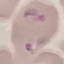

Result: malaria parasites detected. Acquired by smartphone through the microscope eyepiece. Cell patch, automatically extracted from a larger field of view and resized to 64 × 64 pixels. Thin smear of blood. Giemsa-stained preparation.